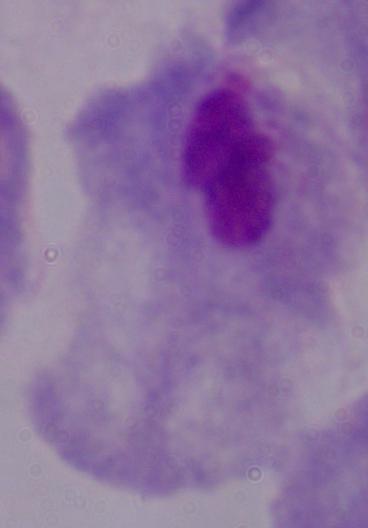

modality: photomicrograph
magnification: 1000x
identification: trichomonad